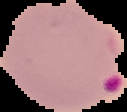

From a thin blood film. Image is 127×112 pixels. Malaria status: parasitized. The area outside the segmented cell region is set to black.